Report the malaria status of this cell.
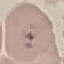

Parasitized.

Thin blood smear. Giemsa stain. Acquired by smartphone through the microscope eyepiece. Automatically extracted cell patch, resized to 64 × 64 pixels.